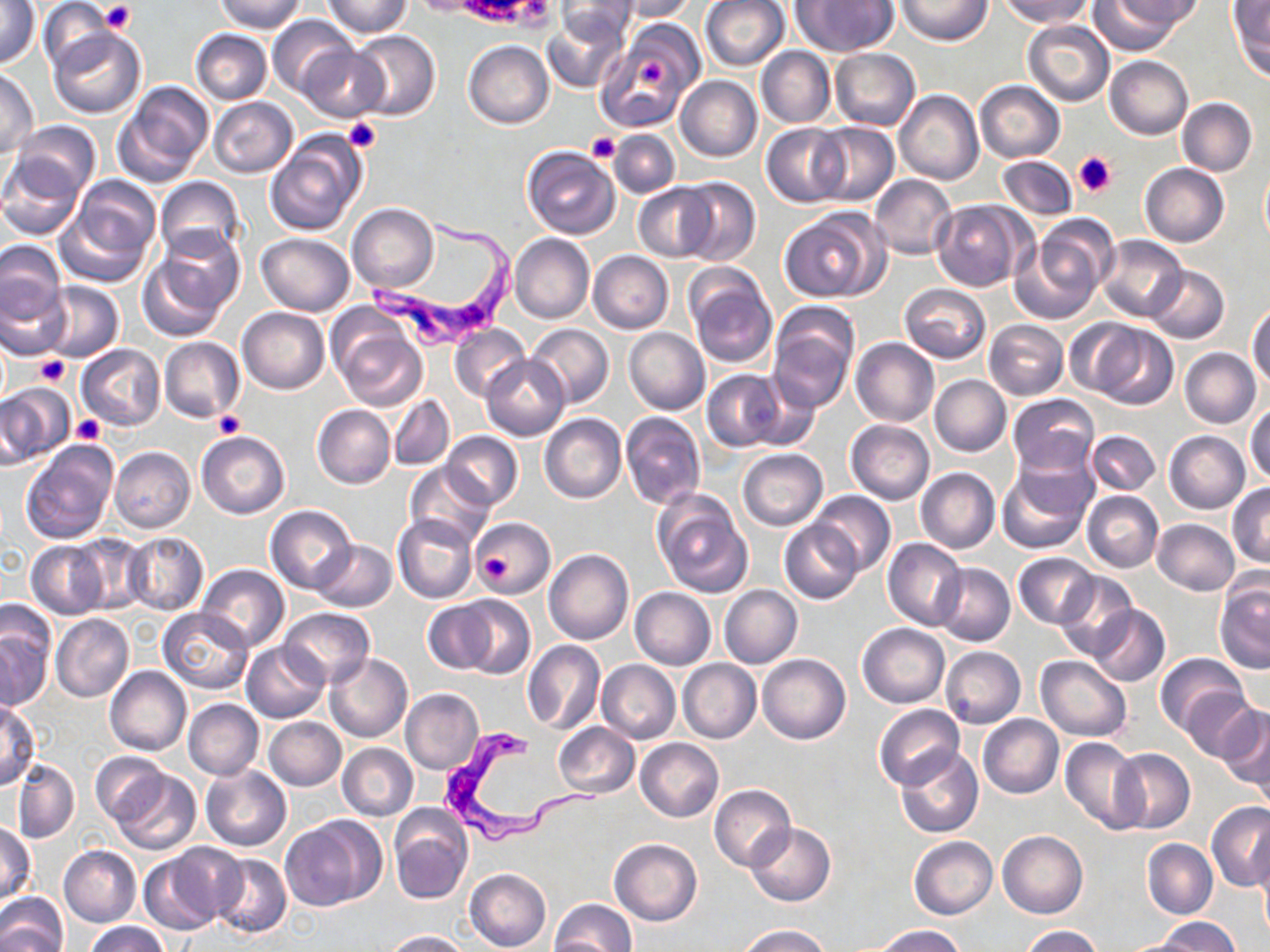
{
  "slide_level_diagnosis": "Trypanosoma brucei",
  "stain": "May-Grünwald-Giemsa",
  "platelet_locations": "approximate bounding boxes as named x1/y1/x2/y2 corners in pixels: (x1=100, y1=2, x2=137, y2=34), (x1=342, y1=118, x2=381, y2=153), (x1=587, y1=132, x2=621, y2=163), (x1=1073, y1=150, x2=1118, y2=197), (x1=33, y1=354, x2=71, y2=385), (x1=213, y1=410, x2=246, y2=438), (x1=73, y1=416, x2=105, y2=445), (x1=475, y1=541, x2=518, y2=588)",
  "image_size": "1270×952 pixels",
  "field_of_view": "one of a larger specimen",
  "magnification": "1000x",
  "uninfected_red_blood_cell_locations": "approximate bounding boxes as named x1/y1/x2/y2 corners in pixels: (x1=214, y1=0, x2=307, y2=34), (x1=557, y1=0, x2=634, y2=45), (x1=615, y1=0, x2=697, y2=21), (x1=700, y1=0, x2=790, y2=71), (x1=793, y1=0, x2=896, y2=55), (x1=897, y1=0, x2=991, y2=46), (x1=1120, y1=0, x2=1204, y2=27), (x1=1229, y1=0, x2=1270, y2=78), (x1=2, y1=1, x2=40, y2=70), (x1=38, y1=1, x2=115, y2=71), (x1=322, y1=1, x2=410, y2=38), (x1=1000, y1=1, x2=1091, y2=26), (x1=1086, y1=1, x2=1183, y2=53), (x1=267, y1=13, x2=357, y2=97), (x1=544, y1=13, x2=628, y2=92), (x1=603, y1=19, x2=702, y2=124), (x1=1021, y1=19, x2=1113, y2=106), (x1=47, y1=28, x2=145, y2=120), (x1=191, y1=30, x2=272, y2=104), (x1=349, y1=31, x2=440, y2=120), (x1=464, y1=41, x2=553, y2=128), (x1=757, y1=45, x2=835, y2=127), (x1=299, y1=46, x2=389, y2=121), (x1=830, y1=48, x2=921, y2=131), (x1=1104, y1=56, x2=1192, y2=140), (x1=0, y1=69, x2=39, y2=157), (x1=675, y1=75, x2=762, y2=162), (x1=975, y1=80, x2=1065, y2=163), (x1=114, y1=82, x2=213, y2=187), (x1=895, y1=90, x2=984, y2=185), (x1=208, y1=97, x2=299, y2=178), (x1=1176, y1=98, x2=1257, y2=175), (x1=9, y1=120, x2=101, y2=202), (x1=810, y1=122, x2=899, y2=205), (x1=762, y1=123, x2=848, y2=207), (x1=609, y1=130, x2=681, y2=198), (x1=266, y1=132, x2=368, y2=236), (x1=521, y1=145, x2=620, y2=239), (x1=998, y1=155, x2=1077, y2=220), (x1=0, y1=156, x2=87, y2=240), (x1=1140, y1=162, x2=1228, y2=246), (x1=1260, y1=165, x2=1270, y2=248), (x1=868, y1=174, x2=958, y2=260), (x1=155, y1=176, x2=245, y2=263), (x1=676, y1=178, x2=760, y2=266), (x1=58, y1=180, x2=160, y2=286), (x1=633, y1=185, x2=716, y2=261), (x1=931, y1=200, x2=1030, y2=291), (x1=347, y1=203, x2=438, y2=292), (x1=778, y1=207, x2=888, y2=303), (x1=1015, y1=221, x2=1114, y2=320), (x1=152, y1=225, x2=245, y2=319), (x1=256, y1=233, x2=355, y2=315), (x1=509, y1=234, x2=593, y2=323), (x1=1095, y1=235, x2=1186, y2=320), (x1=0, y1=241, x2=67, y2=325), (x1=588, y1=250, x2=673, y2=333), (x1=137, y1=252, x2=232, y2=343), (x1=1144, y1=265, x2=1228, y2=343), (x1=686, y1=270, x2=777, y2=368), (x1=0, y1=278, x2=71, y2=361), (x1=38, y1=280, x2=123, y2=362), (x1=898, y1=283, x2=992, y2=362), (x1=1248, y1=302, x2=1270, y2=390), (x1=766, y1=306, x2=858, y2=410), (x1=237, y1=307, x2=329, y2=393), (x1=328, y1=311, x2=429, y2=413), (x1=984, y1=319, x2=1068, y2=400), (x1=525, y1=323, x2=614, y2=408), (x1=1088, y1=323, x2=1178, y2=409), (x1=450, y1=324, x2=529, y2=402), (x1=624, y1=328, x2=710, y2=415), (x1=159, y1=336, x2=244, y2=422), (x1=850, y1=337, x2=939, y2=427), (x1=77, y1=344, x2=165, y2=430), (x1=1178, y1=347, x2=1260, y2=428), (x1=481, y1=355, x2=569, y2=438), (x1=702, y1=370, x2=783, y2=451), (x1=930, y1=374, x2=1011, y2=456), (x1=746, y1=376, x2=824, y2=452), (x1=0, y1=383, x2=71, y2=465), (x1=390, y1=394, x2=454, y2=469), (x1=1008, y1=394, x2=1098, y2=475), (x1=1247, y1=402, x2=1270, y2=484), (x1=312, y1=404, x2=395, y2=489), (x1=620, y1=412, x2=706, y2=510), (x1=540, y1=413, x2=626, y2=503), (x1=846, y1=420, x2=934, y2=503), (x1=197, y1=430, x2=290, y2=518), (x1=1165, y1=430, x2=1250, y2=514), (x1=441, y1=431, x2=522, y2=510), (x1=1087, y1=431, x2=1161, y2=495), (x1=21, y1=440, x2=118, y2=546), (x1=109, y1=446, x2=195, y2=533), (x1=737, y1=448, x2=827, y2=530), (x1=406, y1=462, x2=495, y2=550), (x1=997, y1=462, x2=1094, y2=555), (x1=916, y1=468, x2=1000, y2=554), (x1=1228, y1=484, x2=1270, y2=568), (x1=653, y1=490, x2=753, y2=597), (x1=810, y1=490, x2=895, y2=576), (x1=1082, y1=491, x2=1163, y2=572), (x1=265, y1=505, x2=357, y2=594), (x1=393, y1=514, x2=478, y2=605), (x1=470, y1=518, x2=555, y2=595), (x1=1152, y1=518, x2=1240, y2=595), (x1=779, y1=522, x2=862, y2=602), (x1=122, y1=533, x2=209, y2=615), (x1=71, y1=534, x2=152, y2=615), (x1=883, y1=537, x2=967, y2=630), (x1=311, y1=539, x2=397, y2=612), (x1=27, y1=541, x2=108, y2=618), (x1=544, y1=550, x2=634, y2=645), (x1=1014, y1=552, x2=1100, y2=628), (x1=933, y1=563, x2=1015, y2=646), (x1=197, y1=564, x2=289, y2=652), (x1=1055, y1=570, x2=1139, y2=660), (x1=1215, y1=580, x2=1269, y2=675), (x1=719, y1=585, x2=802, y2=668), (x1=629, y1=587, x2=715, y2=669), (x1=448, y1=595, x2=534, y2=679), (x1=424, y1=600, x2=500, y2=673), (x1=0, y1=601, x2=56, y2=679), (x1=1089, y1=605, x2=1169, y2=686), (x1=159, y1=608, x2=253, y2=693), (x1=279, y1=608, x2=374, y2=690), (x1=51, y1=614, x2=134, y2=703), (x1=858, y1=624, x2=949, y2=707), (x1=1, y1=631, x2=50, y2=710), (x1=242, y1=641, x2=329, y2=723), (x1=522, y1=641, x2=605, y2=733), (x1=940, y1=646, x2=1025, y2=728), (x1=325, y1=651, x2=413, y2=743), (x1=1155, y1=653, x2=1248, y2=738), (x1=757, y1=654, x2=850, y2=743), (x1=1036, y1=655, x2=1131, y2=741), (x1=678, y1=659, x2=761, y2=743), (x1=597, y1=660, x2=680, y2=744), (x1=104, y1=665, x2=191, y2=756), (x1=1182, y1=687, x2=1258, y2=763), (x1=401, y1=689, x2=484, y2=775), (x1=183, y1=699, x2=263, y2=780), (x1=0, y1=701, x2=41, y2=788), (x1=875, y1=704, x2=963, y2=789), (x1=1217, y1=705, x2=1270, y2=792), (x1=978, y1=714, x2=1064, y2=798), (x1=264, y1=717, x2=346, y2=790), (x1=553, y1=722, x2=639, y2=798), (x1=1252, y1=729, x2=1270, y2=815), (x1=1059, y1=737, x2=1144, y2=833), (x1=635, y1=739, x2=724, y2=821), (x1=338, y1=743, x2=418, y2=821), (x1=896, y1=746, x2=982, y2=838), (x1=1109, y1=748, x2=1195, y2=835), (x1=89, y1=753, x2=168, y2=825), (x1=11, y1=760, x2=80, y2=843), (x1=201, y1=764, x2=291, y2=851), (x1=108, y1=770, x2=200, y2=855), (x1=709, y1=785, x2=795, y2=869), (x1=1207, y1=801, x2=1270, y2=891), (x1=389, y1=806, x2=472, y2=904), (x1=280, y1=817, x2=376, y2=911), (x1=745, y1=822, x2=835, y2=906), (x1=1, y1=824, x2=35, y2=901), (x1=998, y1=830, x2=1087, y2=918), (x1=1254, y1=833, x2=1270, y2=930), (x1=909, y1=836, x2=997, y2=919), (x1=609, y1=839, x2=702, y2=926), (x1=1143, y1=839, x2=1217, y2=919), (x1=59, y1=846, x2=141, y2=926), (x1=140, y1=848, x2=230, y2=935), (x1=210, y1=853, x2=291, y2=939), (x1=465, y1=868, x2=552, y2=951), (x1=0, y1=891, x2=66, y2=952), (x1=550, y1=899, x2=636, y2=952), (x1=1157, y1=917, x2=1240, y2=951), (x1=84, y1=922, x2=167, y2=952), (x1=736, y1=925, x2=833, y2=952), (x1=875, y1=925, x2=965, y2=951), (x1=1021, y1=926, x2=1104, y2=952), (x1=384, y1=930, x2=467, y2=951), (x1=1118, y1=934, x2=1203, y2=952)",
  "preparation": "thin blood smear",
  "trypanosoma_brucei_locations": "approximate bounding boxes as named x1/y1/x2/y2 corners in pixels: (x1=361, y1=216, x2=523, y2=357), (x1=437, y1=729, x2=604, y2=843)",
  "modality": "light microscopy"
}